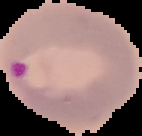
malaria status = parasitized
image size = 142×136 pixels
image type = segmented cell region on a black background
preparation = thin blood smear